Point out each malaria parasite.
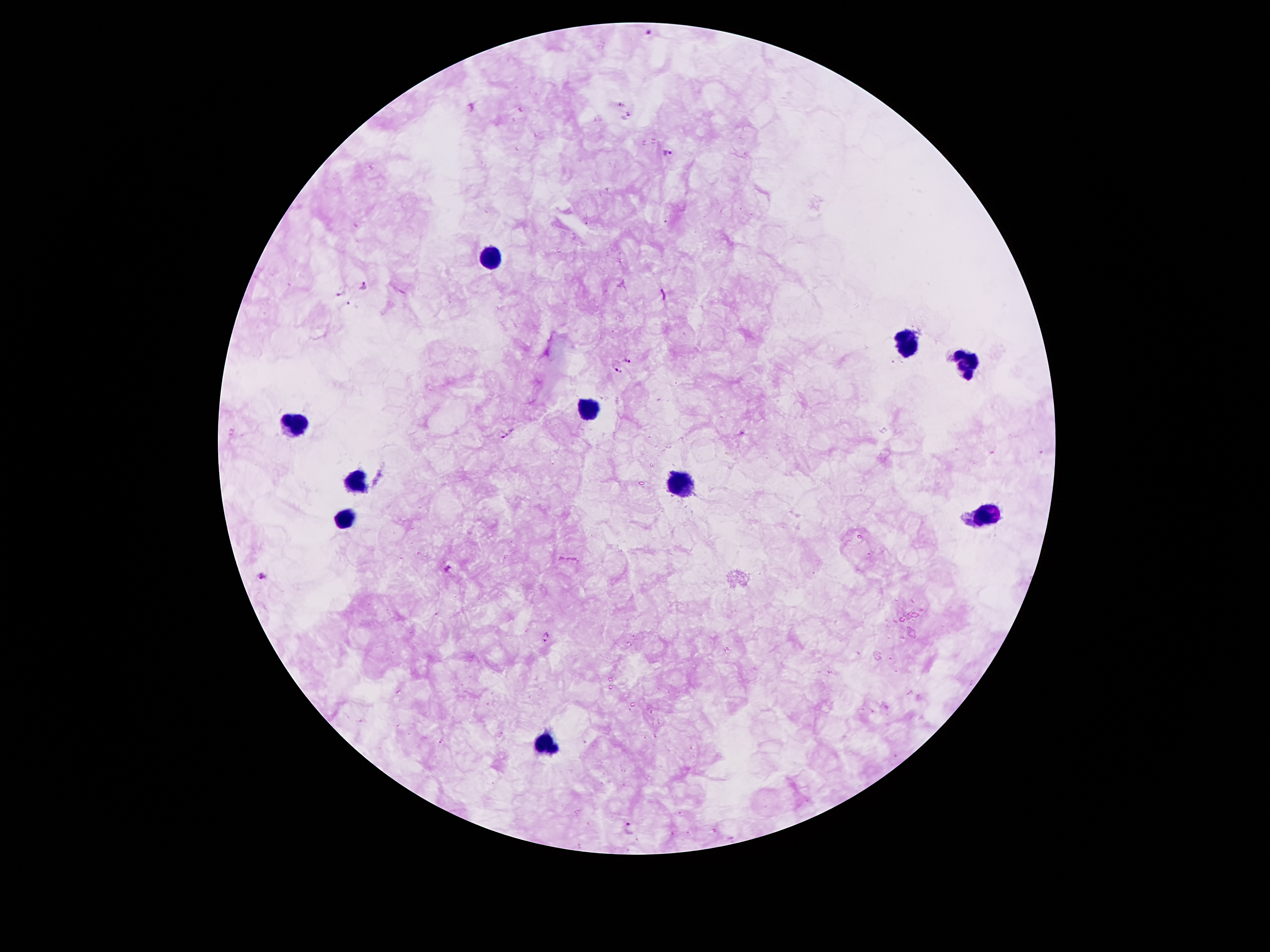
Approximate centers as (x, y) in pixels.
Malaria parasites: (649, 32), (626, 116), (667, 154), (363, 285), (341, 292), (626, 359), (617, 371), (508, 434), (449, 569), (260, 574), (547, 636), (628, 828).

Summary:
  - Leukocyte locations: (492, 257), (905, 342), (966, 363), (585, 410), (293, 424), (352, 480), (683, 487), (989, 515), (345, 516), (546, 743)
  - Field of view: one from this slide
  - Magnification: 100x
  - Capture: smartphone through the microscope eyepiece
  - Preparation: thick blood film
  - Image size: 1270×952 pixels
  - Stain: Giemsa
  - Patient malaria status: positive for Plasmodium falciparum